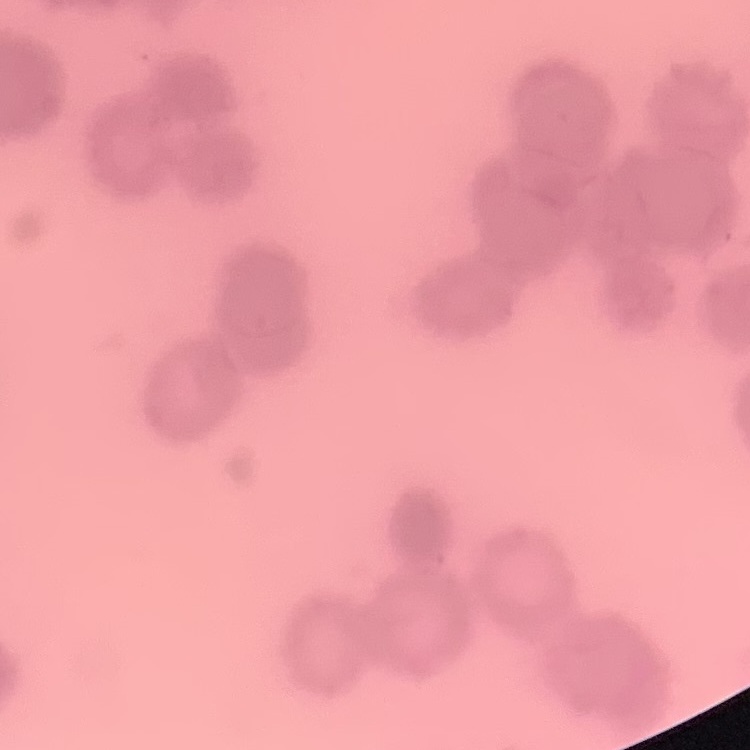

red blood cell morphology = rouleaux formation
stain = Field's or Giemsa
preparation = thin peripheral smear
image type = square crop of a larger photomicrograph